Outline each blood parasite and name the species.
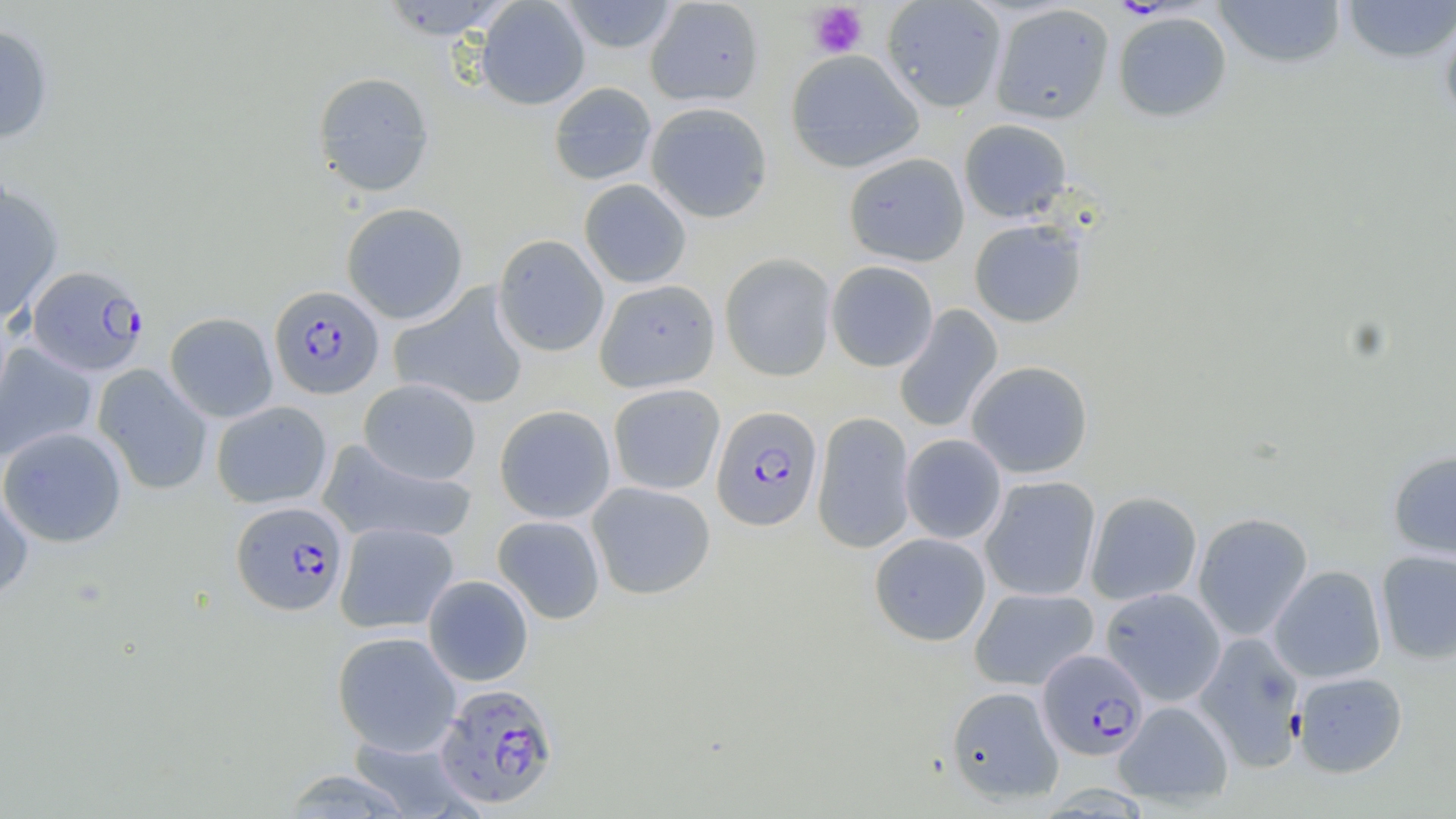

Approximate bounding boxes as [x1, y1, x2, y2] in pixels.
Plasmodium falciparum-infected red blood cells: [26, 265, 149, 377], [269, 284, 385, 399], [711, 405, 823, 531], [231, 500, 349, 616], [1038, 649, 1148, 760], [433, 682, 560, 810].
No Plasmodium ovale, Plasmodium malariae, Plasmodium vivax, Babesia divergens, or Trypanosoma brucei observed.

Platelet locations: [807, 2, 868, 59]. Uninfected red blood cell locations: [378, 0, 514, 40], [476, 0, 590, 110], [644, 0, 765, 107], [1214, 0, 1347, 70], [1340, 0, 1456, 65], [557, 1, 681, 53], [881, 1, 1006, 113], [990, 3, 1114, 125], [1112, 11, 1232, 123], [1440, 14, 1456, 129], [0, 23, 54, 144], [785, 49, 925, 173], [312, 71, 435, 197], [548, 82, 657, 185], [645, 101, 773, 223], [958, 118, 1072, 222], [843, 152, 970, 267], [579, 179, 691, 288], [0, 183, 64, 322], [341, 202, 469, 324], [968, 219, 1087, 327], [493, 234, 609, 357], [719, 253, 836, 382], [825, 260, 938, 372], [594, 278, 720, 393], [389, 284, 529, 410], [894, 304, 1003, 434], [164, 312, 278, 423], [0, 342, 98, 462], [966, 360, 1093, 478], [93, 364, 213, 495], [359, 379, 481, 484], [608, 383, 725, 495], [211, 401, 332, 509], [494, 405, 616, 523], [812, 411, 915, 554], [0, 426, 127, 548], [900, 434, 1007, 544], [317, 439, 476, 547], [1387, 450, 1456, 560], [980, 475, 1101, 602], [587, 481, 716, 600], [0, 483, 34, 605], [1085, 491, 1202, 605], [1192, 512, 1313, 641], [492, 514, 605, 624], [335, 521, 459, 634], [869, 532, 991, 646], [1375, 550, 1456, 664], [1268, 565, 1387, 683], [423, 575, 534, 686], [969, 587, 1099, 691], [1100, 587, 1227, 706], [332, 631, 461, 756], [1193, 632, 1307, 771], [1291, 671, 1408, 778], [945, 685, 1064, 804], [1114, 700, 1234, 808]. Slide-level diagnosis: Plasmodium falciparum. Captured at 1000x magnification. Light microscopy. May-Grünwald-Giemsa-stained preparation. Thin blood film. Image is 1456×819 pixels. Single field of view.